Comment on the morphology of the erythrocytes.
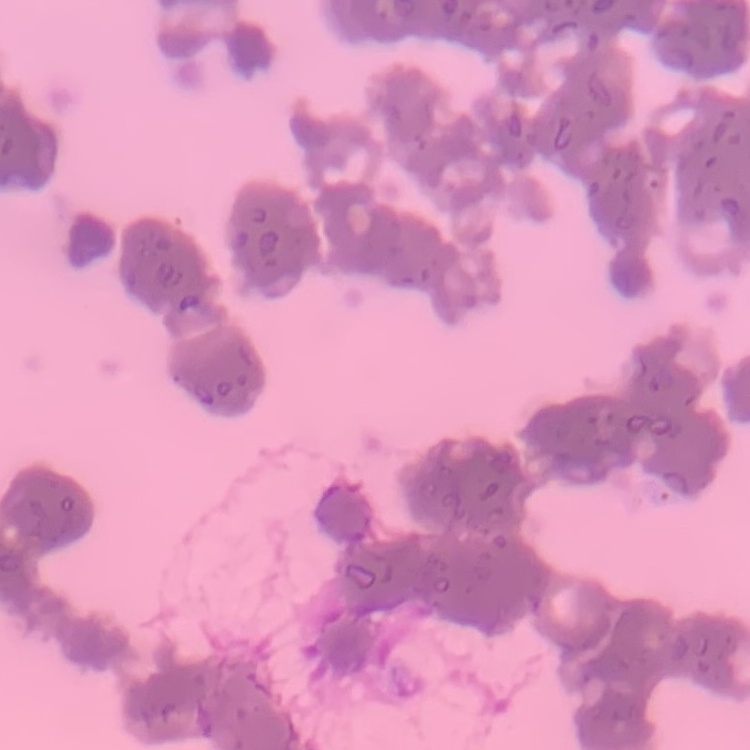
They show rouleaux formation.

{
  "stain": "Field's or Giemsa",
  "preparation": "thin blood smear",
  "image_type": "square crop of a larger photomicrograph"
}